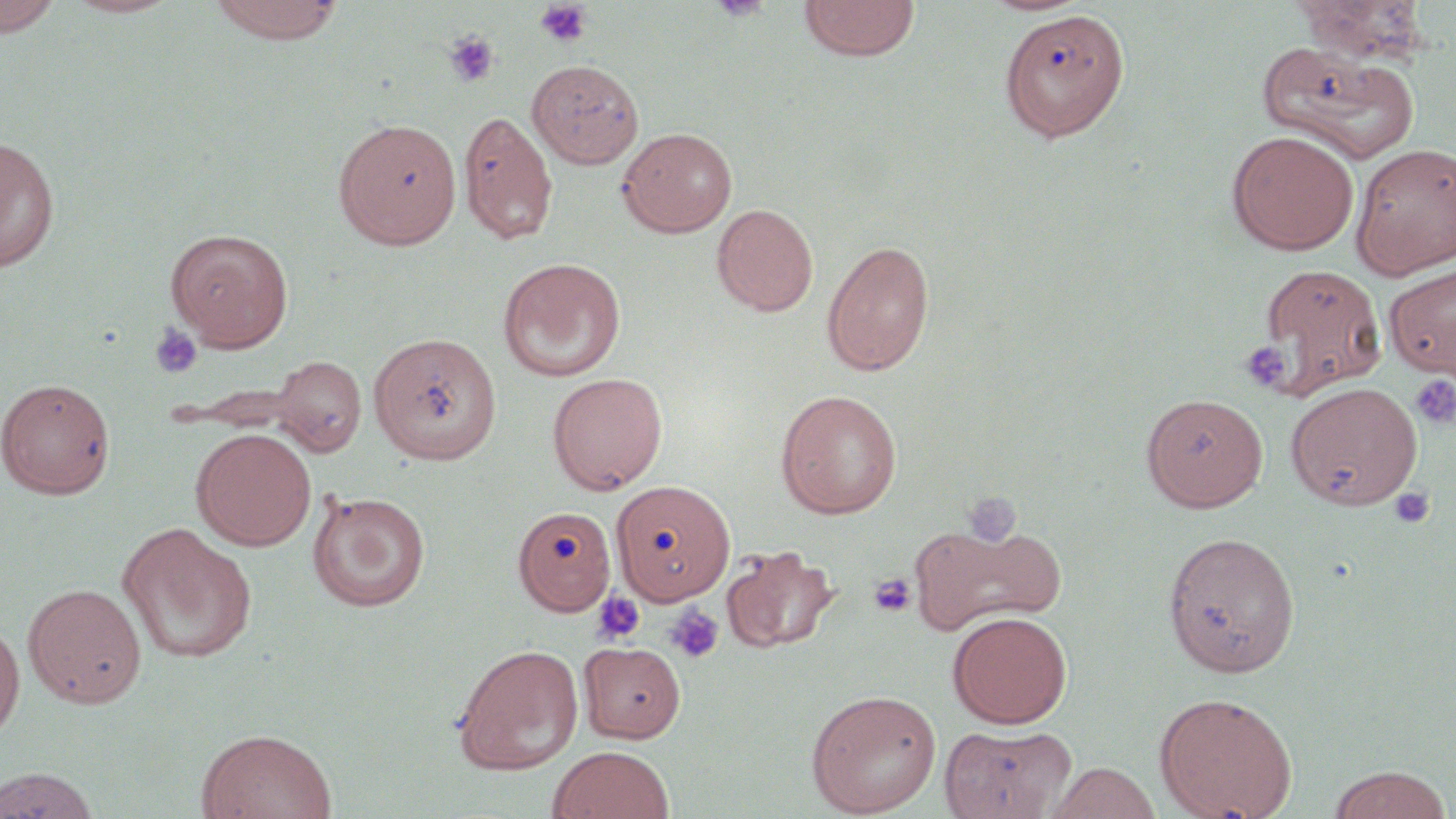
Approximate bounding boxes as [x1, y1, x2, y2] in pixels. Uninfected red blood cell locations (subset): [0, 0, 64, 38], [62, 0, 182, 18], [207, 0, 345, 44], [798, 0, 920, 61], [1294, 0, 1430, 63], [1000, 9, 1130, 142], [1257, 42, 1420, 162], [526, 59, 644, 169], [458, 109, 558, 245], [332, 118, 462, 250], [617, 126, 737, 237], [1227, 130, 1359, 254], [0, 136, 59, 272], [1351, 143, 1456, 280], [712, 203, 818, 317], [166, 228, 294, 351], [821, 238, 935, 377], [498, 257, 626, 382], [1254, 262, 1389, 398], [1385, 264, 1456, 378], [368, 331, 502, 464], [270, 355, 366, 457], [547, 372, 668, 494], [1, 377, 116, 499], [1285, 381, 1423, 510], [775, 389, 903, 519], [1140, 392, 1269, 511], [192, 427, 316, 551], [610, 479, 736, 605], [308, 490, 431, 612], [512, 505, 617, 616], [909, 519, 1066, 638], [116, 522, 258, 664], [1162, 531, 1301, 677], [721, 544, 840, 654], [23, 583, 147, 708], [948, 611, 1072, 728], [0, 619, 24, 741], [578, 641, 687, 743], [451, 643, 584, 776], [805, 689, 942, 817], [1154, 692, 1298, 819], [938, 723, 1076, 819], [196, 728, 338, 819], [547, 746, 675, 819], [1046, 762, 1162, 819], [1327, 765, 1454, 819], [1, 768, 102, 818]. Platelet locations (subset): [535, 1, 593, 48], [444, 32, 500, 87], [149, 323, 203, 379], [1240, 341, 1292, 393], [1410, 375, 1456, 430], [1388, 486, 1436, 530], [867, 572, 917, 618], [591, 590, 646, 646], [665, 603, 725, 664]. Slide-level diagnosis: negative for blood parasites. Captured at 1000x magnification. Thin blood film. Optical microscopy. May-Grünwald-Giemsa stain. Image is 1456×819 pixels. One field of a larger specimen.